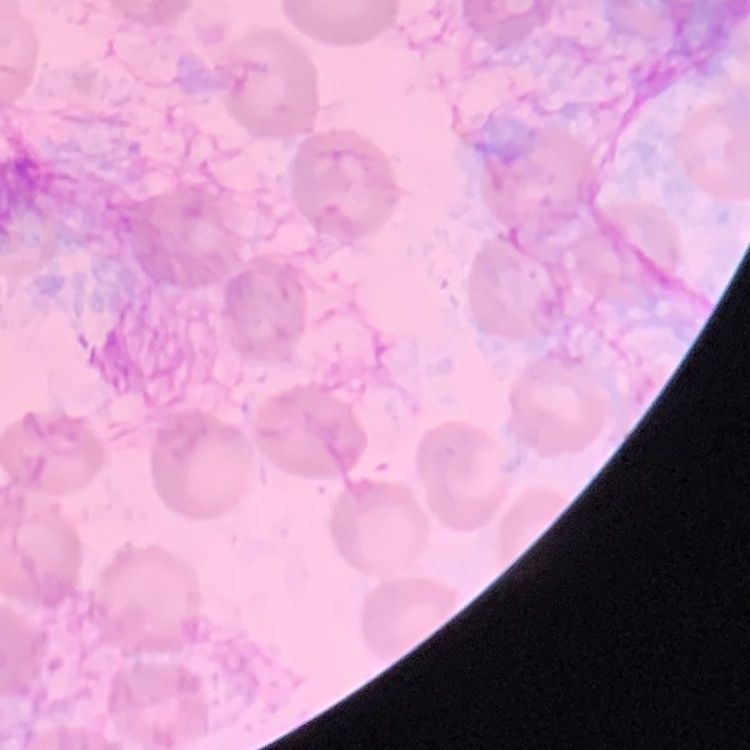
erythrocyte morphology = no rouleaux formation
preparation = thin blood smear
stain = Field's or Giemsa
image type = one tile cut from a larger photomicrograph